Assess this cell for malaria.
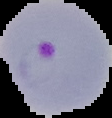

Parasitized.

From a thin blood film. Image is 112×118 pixels. Segmented cell region on a black background.